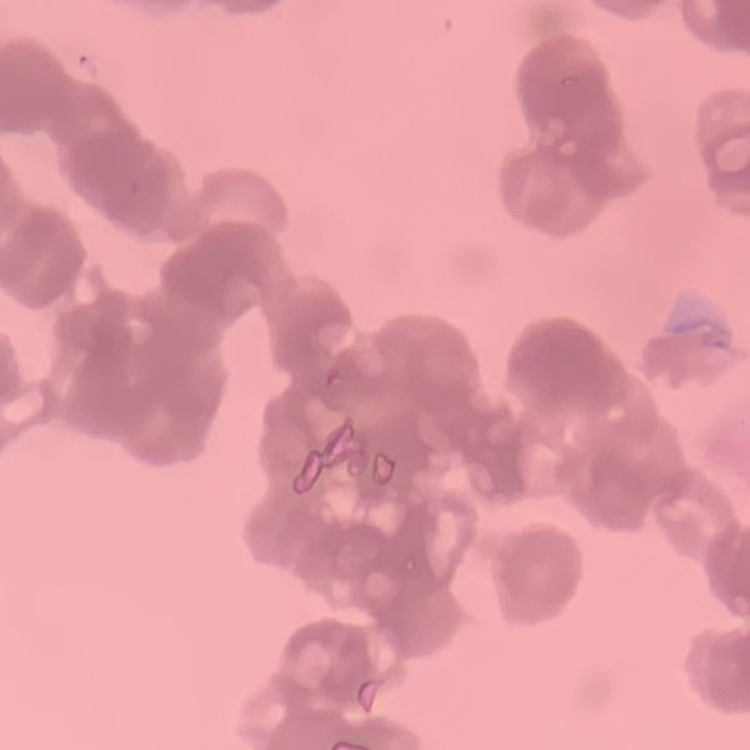

red blood cell morphology = rouleaux formation
preparation = thin blood film
image type = one tile cut from a larger photomicrograph
stain = Field's or Giemsa